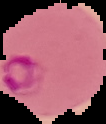
Summary:
  - Malaria status: parasitized
  - Preparation: thin blood smear
  - Image size: 106×124 pixels
  - Image type: segmented cell region with the area outside set to black